Name the parasite shown.
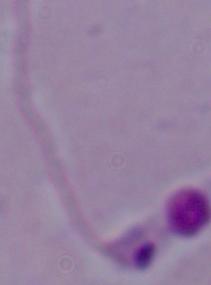

This is Leishmania.

magnification = 1000x
modality = micrograph